Locate and identify every blood parasite.
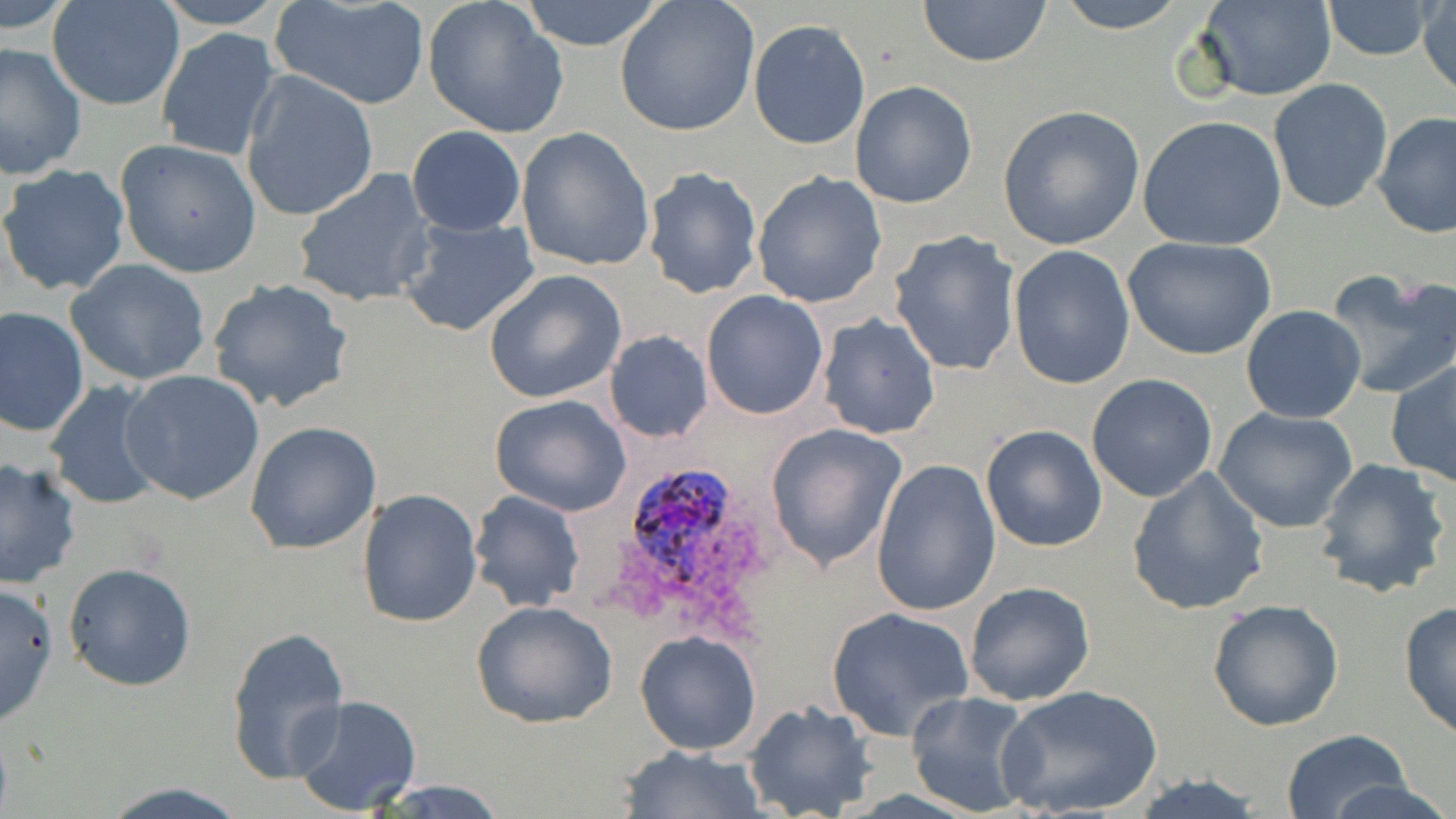
Approximate bounding boxes as [x1, y1, x2, y2] in pixels.
Plasmodium ovale-infected red blood cells: [627, 469, 730, 590].
No Plasmodium falciparum, Plasmodium malariae, Plasmodium vivax, Babesia divergens, or Trypanosoma brucei observed.

{
  "slide_level_diagnosis": "Plasmodium ovale",
  "preparation": "thin blood smear",
  "stain": "May-Grünwald-Giemsa",
  "field_of_view": "single",
  "image_size": "1456×819 pixels",
  "magnification": "1000x",
  "modality": "light microscopy",
  "uninfected_red_blood_cell_locations": "approximate bounding boxes as [x1, y1, x2, y2] in pixels: [148, 0, 290, 29], [423, 0, 570, 138], [513, 0, 670, 51], [916, 0, 1054, 68], [1050, 0, 1193, 32], [1193, 0, 1337, 102], [1320, 0, 1437, 60], [3, 1, 75, 40], [47, 1, 185, 112], [268, 1, 432, 111], [614, 1, 759, 138], [1418, 2, 1455, 101], [747, 18, 872, 151], [155, 28, 280, 162], [0, 42, 87, 178], [240, 69, 380, 223], [1267, 78, 1396, 216], [849, 81, 978, 209], [997, 104, 1144, 250], [1373, 112, 1456, 239], [1138, 115, 1288, 250], [406, 125, 526, 236], [516, 127, 655, 273], [115, 138, 262, 277], [0, 164, 131, 298], [642, 166, 763, 299], [292, 168, 436, 309], [751, 170, 888, 309], [398, 216, 540, 338], [887, 230, 1023, 378], [1122, 236, 1277, 360], [1008, 246, 1135, 390], [64, 259, 212, 387], [482, 268, 628, 404], [1323, 271, 1456, 400], [207, 277, 353, 413], [701, 290, 829, 420], [0, 305, 89, 437], [1240, 305, 1368, 425], [817, 312, 942, 441], [604, 330, 713, 443], [1385, 360, 1456, 487], [121, 369, 265, 506], [1087, 373, 1218, 503], [45, 381, 169, 513], [490, 393, 632, 516], [1213, 408, 1359, 534], [245, 420, 384, 555], [764, 421, 909, 573], [979, 424, 1110, 553], [1311, 455, 1452, 599], [0, 457, 81, 591], [871, 458, 1002, 615], [1126, 467, 1271, 616], [358, 488, 482, 628], [469, 491, 586, 613], [63, 563, 197, 691], [0, 580, 60, 726], [964, 580, 1095, 705], [1206, 599, 1344, 730], [471, 600, 618, 728], [1398, 600, 1456, 741], [826, 607, 973, 740], [225, 624, 351, 786], [635, 631, 763, 756], [998, 684, 1161, 817], [904, 690, 1040, 817], [289, 695, 422, 816], [743, 698, 876, 818], [1277, 731, 1417, 818], [617, 745, 765, 818], [1124, 771, 1272, 818], [1331, 778, 1453, 819], [96, 780, 246, 817], [370, 781, 515, 818]"
}